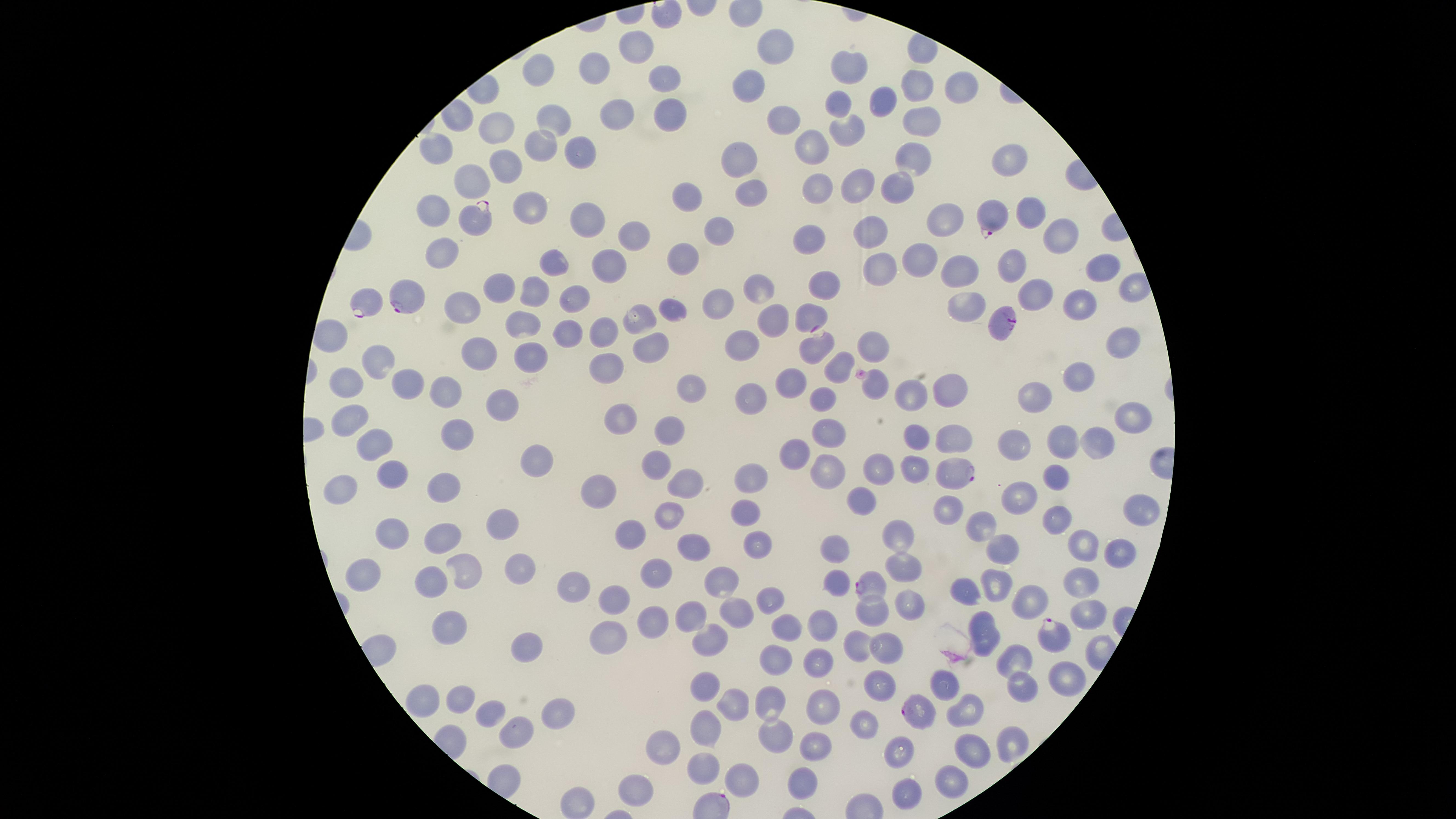

Approximate marker points as (x, y) in pixels.
Summary:
  - Uninfected red blood cells: (774, 46), (632, 47), (537, 66), (594, 68), (853, 68), (669, 76), (917, 85), (961, 88), (747, 89), (839, 98), (875, 100), (615, 111), (671, 112), (552, 117), (847, 122), (919, 122), (785, 123), (497, 124), (815, 138), (540, 143), (436, 146), (582, 152), (736, 156), (912, 157), (505, 161), (1007, 164), (472, 179), (862, 181), (895, 187), (818, 191), (750, 193), (688, 194), (524, 203), (1027, 209), (431, 210), (948, 217), (586, 218), (723, 224), (631, 233), (866, 233), (1054, 238), (813, 239), (440, 251), (685, 254), (552, 261), (919, 264), (960, 264), (608, 265), (1014, 266), (1096, 267), (876, 269), (826, 280), (499, 283), (753, 288), (533, 292), (575, 292), (1030, 297), (714, 302), (1081, 302), (969, 304), (674, 306), (461, 308), (807, 312), (634, 314), (522, 318), (774, 318), (327, 330), (562, 330), (599, 332), (1119, 341), (875, 344), (480, 348), (743, 348), (654, 349), (535, 352), (608, 361), (374, 362), (839, 367), (344, 376), (792, 377), (1073, 377), (450, 381), (873, 382), (946, 384), (411, 385), (689, 390), (1034, 391), (913, 392), (750, 398), (824, 402), (503, 406), (347, 416), (620, 417), (1125, 424), (669, 430), (831, 431), (447, 434), (917, 436), (948, 436), (1086, 439), (366, 441), (1015, 442), (1059, 442), (797, 447), (658, 459), (539, 461), (910, 467), (873, 470), (390, 473), (826, 473), (1058, 478), (748, 481), (684, 482), (447, 484), (334, 487), (602, 491), (1021, 494), (862, 498), (1143, 503), (951, 506), (746, 511), (678, 512), (1056, 512), (507, 517), (985, 526), (441, 534), (898, 537), (397, 539), (633, 539), (1076, 544), (836, 545), (1004, 545), (696, 546), (759, 546), (1117, 554), (904, 564), (519, 565), (466, 569), (653, 570), (366, 578), (720, 579), (432, 583), (998, 583), (838, 584), (1079, 585), (579, 588), (963, 592), (617, 595), (762, 596), (1030, 600), (910, 601), (1087, 611), (736, 612), (870, 615), (984, 617), (693, 618), (820, 623), (655, 626), (786, 626), (451, 631), (604, 635), (708, 636), (858, 641), (884, 644), (985, 646), (524, 649), (1018, 658), (819, 662), (773, 664), (1072, 675), (881, 683), (947, 684), (1021, 685), (707, 688), (458, 696), (416, 698), (823, 704), (736, 705), (765, 705), (964, 709), (489, 710), (555, 713), (864, 727), (519, 730), (709, 731), (1012, 740), (766, 741), (818, 743), (662, 747), (969, 747), (894, 753), (703, 771), (744, 778), (949, 779), (802, 781), (633, 788), (898, 798), (578, 804)
  - Parasitized red blood cells: (471, 219), (992, 219), (402, 295), (370, 302), (1003, 322), (819, 352), (950, 469), (875, 586), (1055, 635), (917, 708)
  - Capture: smartphone photograph through the microscope eyepiece
  - Presence: malaria parasites detected
  - Visible region: circular
  - Field of view: single
  - Species: Plasmodium falciparum
  - Image size: 1456×819 pixels
  - Preparation: thin smear of blood
  - Stain: Giemsa